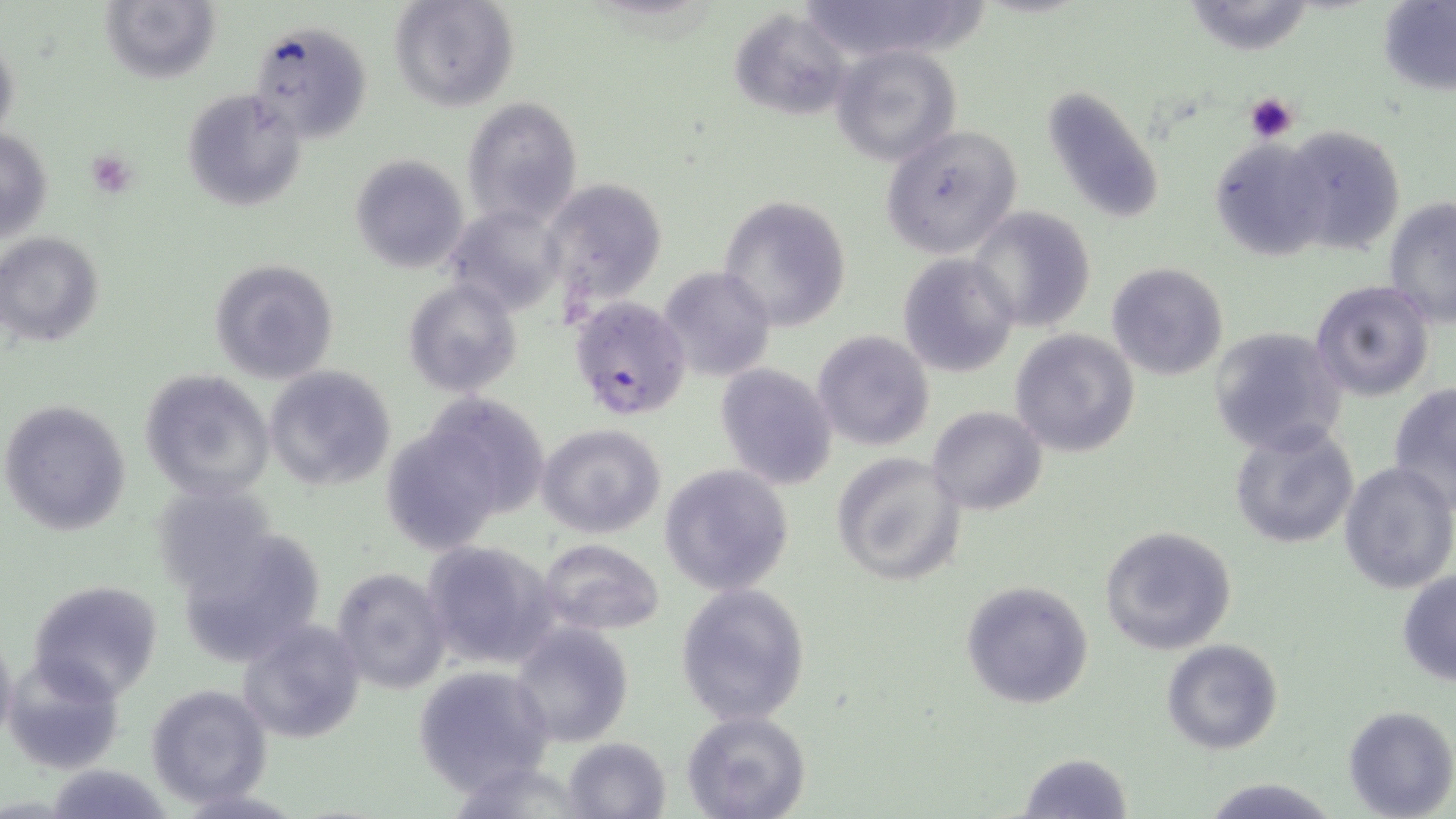
Summary:
  - Coordinate format: approximate bounding boxes as [x1, y1, x2, y2] in pixels
  - Uninfected red blood cell locations: [391, 0, 519, 112], [809, 0, 973, 71], [1180, 0, 1319, 55], [99, 1, 220, 84], [1376, 2, 1455, 95], [729, 9, 850, 119], [247, 19, 374, 143], [0, 32, 21, 153], [831, 44, 961, 166], [1041, 82, 1165, 227], [182, 90, 307, 211], [462, 97, 582, 230], [880, 125, 1024, 259], [1276, 125, 1407, 253], [1, 127, 52, 245], [1207, 139, 1327, 260], [350, 154, 470, 274], [541, 177, 667, 310], [718, 196, 852, 332], [1381, 201, 1454, 324], [445, 203, 567, 318], [969, 206, 1096, 333], [0, 232, 105, 348], [897, 253, 1020, 377], [209, 259, 338, 384], [1106, 262, 1230, 380], [658, 265, 776, 381], [403, 277, 523, 399], [1310, 280, 1436, 402], [1207, 325, 1351, 455], [1010, 329, 1139, 458], [812, 330, 935, 451], [715, 363, 837, 489], [262, 365, 398, 492], [139, 370, 275, 501], [1388, 382, 1456, 510], [418, 392, 553, 520], [0, 398, 133, 538], [927, 406, 1048, 515], [1228, 422, 1360, 550], [535, 423, 667, 538], [830, 451, 966, 588], [1337, 460, 1455, 594], [659, 464, 796, 597], [150, 480, 282, 594], [176, 524, 329, 670], [1098, 524, 1237, 655], [420, 540, 559, 669], [536, 540, 666, 636], [331, 566, 452, 694], [1396, 568, 1456, 688], [27, 579, 164, 702], [960, 580, 1094, 709], [675, 581, 809, 725], [237, 618, 367, 742], [510, 623, 635, 749], [0, 627, 18, 753], [1160, 638, 1284, 755], [3, 656, 125, 775], [412, 663, 555, 795], [145, 684, 272, 806], [1342, 705, 1456, 819], [682, 711, 812, 819], [562, 736, 672, 819], [1017, 750, 1133, 819], [447, 759, 595, 818], [1204, 777, 1335, 818]
  - Platelet locations: [1244, 90, 1299, 142], [85, 150, 139, 199]
  - Plasmodium falciparum-infected red blood cell locations: [568, 295, 692, 421]
  - Slide-level diagnosis: Plasmodium falciparum
  - Field of view: one of a larger specimen
  - Magnification: 1000x
  - Image size: 1456×819 pixels
  - Preparation: thin blood smear
  - Modality: optical microscopy
  - Stain: May-Grünwald-Giemsa